Identify the parasite.
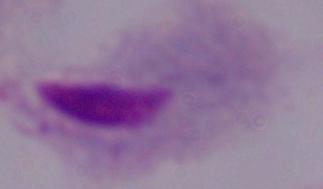
This is a trichomonad.

Micrograph. 1000x magnification.